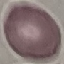
malaria status = uninfected
capture = smartphone camera at the microscope eyepiece
stain = Giemsa
preparation = thin blood film
image type = automatically extracted cell patch, resized to 64 × 64 pixels